Assess this cell for malaria.
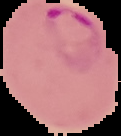

Parasitized.

Segmented cell region on a black background. Image is 121×136 pixels. From a thin blood smear.